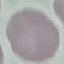
{
  "result": "no malaria parasites detected",
  "image_type": "cell patch, automatically extracted from a larger field of view and resized to 64 × 64 pixels",
  "stain": "Giemsa",
  "capture": "smartphone through the microscope eyepiece",
  "preparation": "thin blood smear"
}